Classify this cell by malaria status.
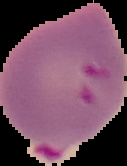
Parasitized.

The area outside the segmented cell region is set to black. Image is 127×166 pixels. From a thin blood smear.